Classify this cell by malaria status.
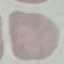
It is uninfected.

Thin smear of blood. Giemsa-stained preparation. Acquired by smartphone through the microscope eyepiece. Cell patch, automatically extracted from a larger field of view and resized to 64 × 64 pixels.